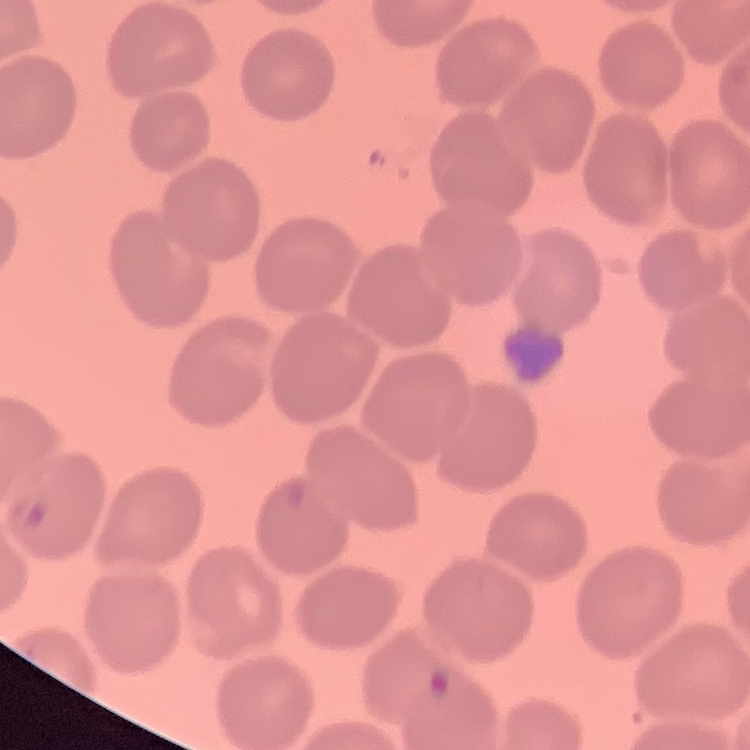

{
  "erythrocyte_morphology": "no rouleaux formation",
  "image_type": "one tile cut from a larger photomicrograph",
  "stain": "Field's or Giemsa",
  "preparation": "thin blood smear"
}